Report the malaria status of this cell.
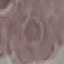
Uninfected.

Summary:
  - Preparation: thin blood film
  - Image type: automatically extracted cell patch, resized to 64 × 64 pixels
  - Stain: Giemsa
  - Capture: smartphone camera at the microscope eyepiece